Identify the cell.
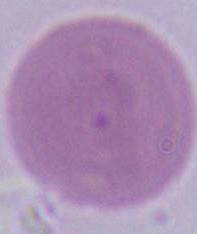
This is an erythrocyte.

Summary:
  - Magnification: 1000x
  - Modality: photomicrograph